Describe the morphology of the red blood cells.
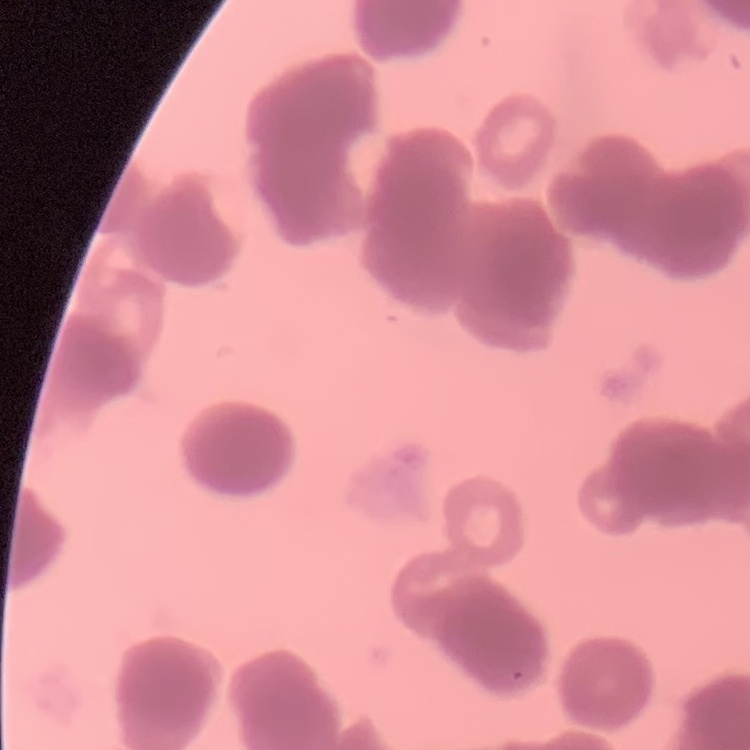
Rouleaux formation.

image type = one tile cut from a larger photomicrograph
stain = Field's or Giemsa
preparation = thin blood film